State which cell type is depicted.
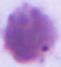
This is an erythrocyte.

{
  "magnification": "1000x",
  "modality": "photomicrograph"
}